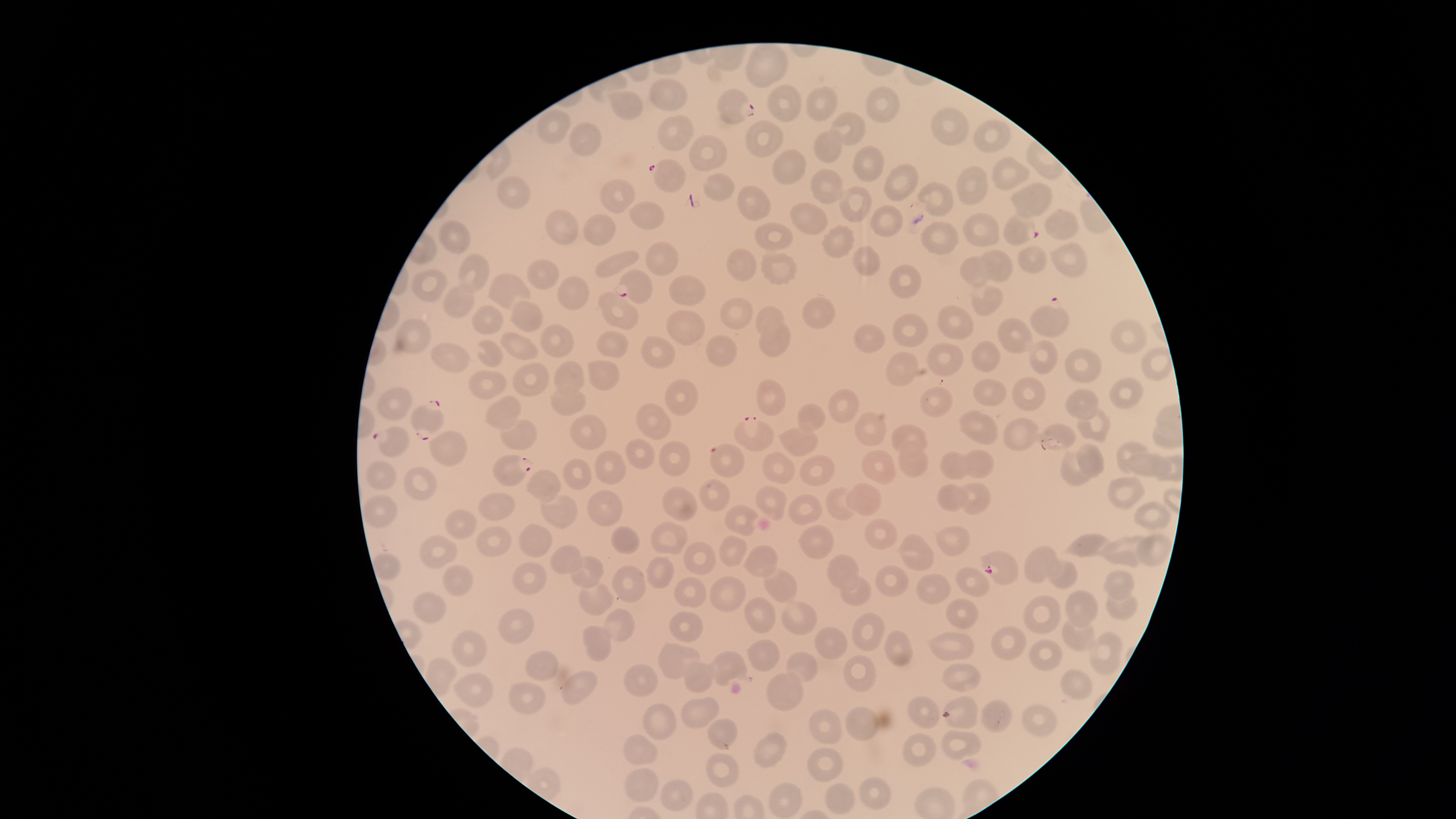

Approximate bounding boxes as [left, top, right, bottom] in pixels. Uninfected RBCs: [745, 44, 788, 88], [648, 77, 688, 110], [768, 85, 802, 122], [866, 85, 899, 124], [806, 86, 837, 122], [606, 91, 643, 119], [930, 106, 971, 146], [538, 110, 569, 144], [831, 111, 865, 145], [657, 115, 694, 150], [744, 119, 783, 158], [973, 122, 1011, 152], [568, 123, 602, 155], [814, 130, 841, 162], [689, 134, 729, 172], [853, 145, 884, 182], [773, 150, 806, 184], [992, 156, 1031, 191], [884, 163, 918, 201], [956, 165, 987, 205], [807, 169, 842, 203], [703, 174, 735, 202], [498, 176, 530, 209], [599, 179, 636, 214], [918, 182, 954, 216], [1009, 182, 1052, 217], [839, 185, 873, 223], [738, 186, 772, 221], [626, 201, 665, 228], [789, 203, 830, 235], [871, 205, 903, 236], [545, 209, 580, 245], [1045, 209, 1078, 239], [583, 212, 617, 245], [962, 212, 1000, 246], [921, 220, 959, 254], [439, 221, 471, 254], [755, 222, 793, 251], [822, 225, 855, 258], [644, 242, 678, 275], [1051, 243, 1087, 277], [854, 245, 881, 277], [1019, 246, 1048, 273], [725, 248, 756, 281], [977, 249, 1012, 281], [595, 250, 639, 278], [761, 253, 797, 284], [459, 254, 493, 293], [960, 256, 989, 286], [528, 259, 559, 289], [890, 264, 923, 299], [411, 269, 448, 303], [487, 273, 530, 312], [558, 275, 589, 310], [668, 275, 708, 304], [446, 284, 477, 320], [969, 284, 1003, 315], [598, 291, 639, 330], [720, 296, 755, 329], [801, 298, 834, 328], [510, 300, 544, 333], [472, 305, 504, 333], [937, 305, 974, 340], [756, 306, 784, 337], [666, 311, 705, 345], [891, 312, 929, 347], [997, 317, 1034, 353], [394, 318, 431, 353], [758, 320, 791, 359], [1111, 320, 1147, 354], [539, 323, 574, 357], [855, 324, 885, 354], [499, 330, 537, 359], [598, 331, 627, 358], [706, 335, 739, 367], [640, 337, 675, 368], [477, 340, 504, 368], [1029, 341, 1057, 374], [972, 342, 999, 372], [926, 343, 963, 377], [431, 344, 469, 372], [1065, 349, 1102, 383], [886, 351, 919, 385], [588, 359, 618, 389], [554, 360, 585, 394], [513, 361, 550, 396], [470, 370, 508, 400], [1011, 376, 1047, 411], [1109, 377, 1145, 410], [756, 379, 787, 417], [973, 379, 1008, 405], [665, 380, 697, 415], [549, 385, 586, 416], [919, 386, 952, 417], [377, 387, 411, 421], [1065, 388, 1100, 421], [829, 390, 859, 423], [485, 395, 521, 429], [797, 404, 825, 432], [637, 405, 671, 438], [1077, 409, 1110, 441], [851, 410, 887, 446], [957, 410, 998, 445], [567, 414, 607, 450], [1003, 418, 1040, 450], [501, 419, 538, 450], [891, 424, 926, 456], [1044, 424, 1075, 447], [779, 425, 818, 455], [428, 430, 469, 467], [626, 439, 655, 471], [657, 440, 692, 475], [899, 441, 929, 477], [1115, 441, 1147, 473], [1076, 443, 1106, 478], [861, 450, 895, 484], [1060, 450, 1091, 486], [594, 451, 624, 485], [762, 451, 795, 484], [939, 451, 968, 479], [965, 451, 993, 478], [1130, 452, 1155, 475], [799, 455, 836, 487], [1154, 456, 1173, 480], [563, 459, 593, 490], [367, 460, 396, 490], [404, 466, 438, 501], [525, 471, 561, 502], [1107, 476, 1145, 510], [700, 480, 731, 509], [846, 482, 883, 515], [956, 483, 990, 515], [936, 485, 967, 512], [662, 487, 698, 520], [756, 487, 786, 521], [826, 487, 858, 520], [588, 491, 624, 525], [477, 492, 516, 520], [361, 495, 397, 527], [540, 495, 579, 530], [788, 495, 821, 525], [1134, 501, 1171, 528], [725, 506, 758, 537], [445, 508, 476, 539], [865, 518, 896, 552], [652, 521, 688, 554], [518, 524, 552, 555], [798, 525, 834, 558], [477, 526, 512, 556], [611, 526, 640, 553], [936, 526, 970, 556], [900, 534, 935, 571], [1062, 534, 1112, 558], [1136, 534, 1171, 566], [419, 535, 457, 570], [720, 535, 749, 566], [1096, 535, 1151, 566], [683, 541, 715, 574], [550, 544, 582, 574], [744, 545, 778, 578], [1024, 546, 1062, 583], [373, 553, 401, 580], [826, 554, 858, 591], [646, 556, 675, 588], [570, 557, 604, 589], [1048, 560, 1079, 590], [514, 564, 547, 594], [443, 565, 473, 597], [614, 565, 645, 603], [875, 566, 908, 599], [762, 567, 797, 603], [955, 568, 990, 598], [1104, 569, 1135, 598], [916, 573, 951, 604], [709, 576, 747, 611], [841, 576, 870, 606], [674, 578, 707, 606], [579, 582, 613, 616], [412, 590, 447, 622], [1066, 590, 1099, 628], [1105, 591, 1136, 619], [1023, 595, 1061, 633], [744, 596, 775, 632], [781, 598, 819, 635], [946, 598, 979, 629], [498, 608, 535, 644], [604, 608, 635, 641], [669, 610, 702, 642], [851, 611, 886, 650], [1062, 616, 1093, 650], [583, 625, 612, 661], [815, 626, 847, 658], [990, 627, 1027, 658], [885, 629, 913, 666], [452, 630, 487, 666], [1088, 631, 1123, 675], [928, 632, 976, 661], [747, 640, 779, 671], [1029, 640, 1063, 671], [658, 643, 700, 679], [526, 650, 560, 682], [786, 651, 818, 682], [711, 652, 746, 685], [844, 654, 877, 692], [683, 662, 713, 692], [941, 662, 981, 691], [625, 664, 659, 697], [1060, 669, 1093, 700], [562, 671, 598, 705], [454, 672, 494, 706], [767, 672, 803, 709], [509, 683, 547, 714], [907, 695, 940, 728], [680, 696, 720, 727], [943, 696, 979, 728], [981, 700, 1013, 732], [1022, 703, 1059, 736], [643, 704, 676, 740], [846, 707, 879, 740], [809, 710, 842, 743], [708, 718, 738, 750], [753, 731, 786, 768], [941, 731, 980, 759], [902, 732, 937, 766], [623, 735, 657, 765], [807, 748, 842, 782], [707, 753, 739, 787], [626, 768, 659, 801], [860, 777, 891, 809], [660, 780, 693, 810], [769, 783, 802, 817], [826, 783, 855, 814]. Parasitized RBCs: [717, 88, 756, 124], [646, 158, 689, 193], [1003, 212, 1039, 246], [616, 270, 652, 304], [1029, 295, 1070, 336], [409, 400, 444, 441], [734, 415, 775, 452], [372, 426, 412, 459], [708, 442, 747, 478], [492, 455, 534, 486], [981, 550, 1018, 584]. Single field of view. The visible region is circular. Photographed with a smartphone camera through the microscope eyepiece. Thin blood smear. Image is 1456×819 pixels. Giemsa-stained preparation. Presence: malaria parasites detected. Species: Plasmodium falciparum.